Locate and identify every blood parasite.
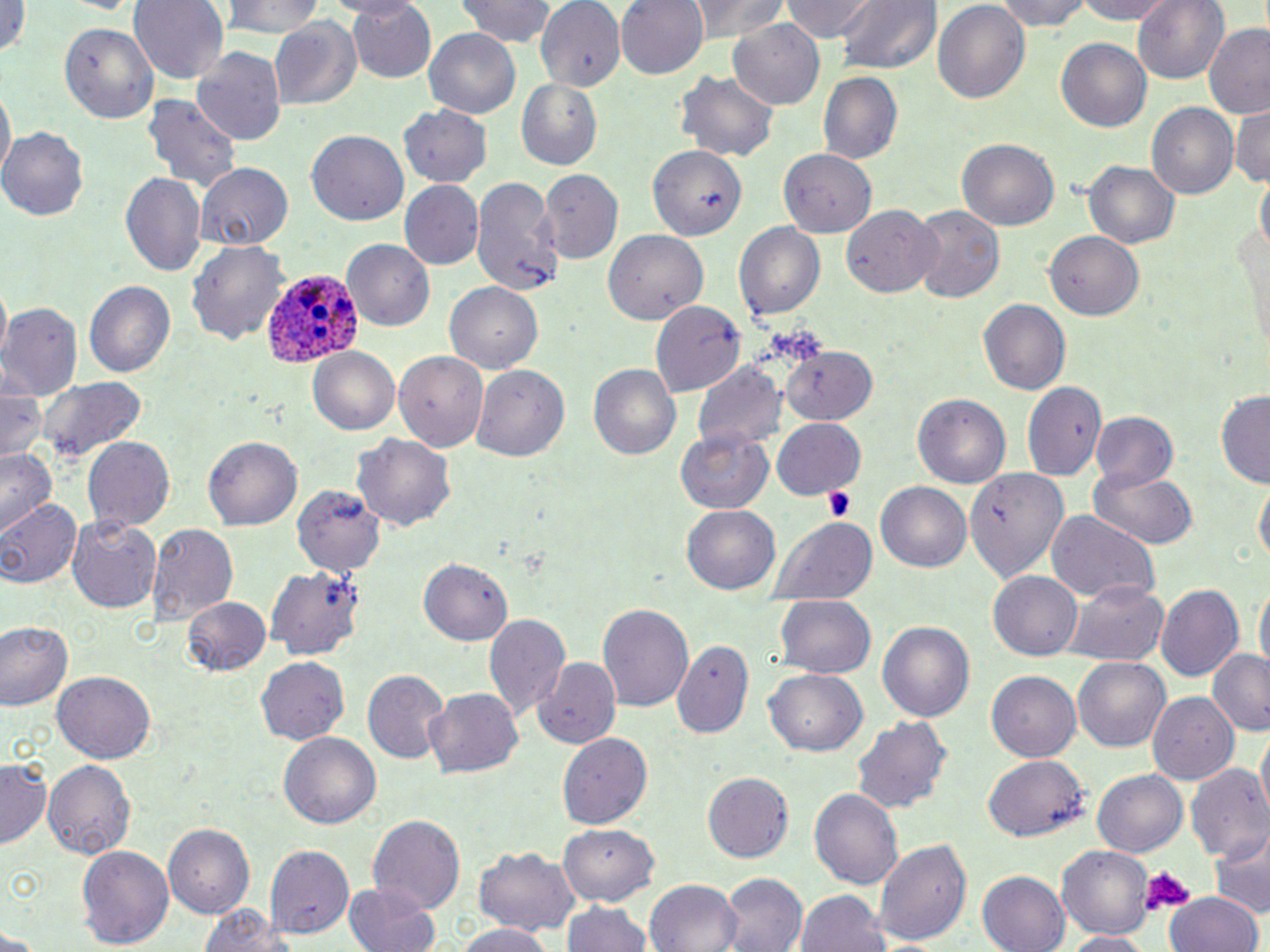
Approximate bounding boxes as (x1, y1, x2, y2) in pixels.
Plasmodium ovale-infected red blood cells: (258, 269, 367, 371).
No Plasmodium falciparum, Plasmodium malariae, Plasmodium vivax, Babesia divergens, or Trypanosoma brucei observed.

Platelet locations: (824, 488, 855, 523), (1140, 865, 1194, 913). Uninfected red blood cell locations: (129, 0, 228, 84), (221, 0, 329, 38), (343, 0, 436, 84), (454, 0, 558, 47), (614, 0, 709, 80), (686, 0, 789, 44), (778, 0, 875, 42), (830, 0, 940, 75), (932, 0, 1032, 105), (992, 0, 1097, 31), (1068, 0, 1179, 23), (1133, 0, 1230, 87), (534, 2, 626, 85), (0, 3, 25, 63), (269, 19, 364, 110), (727, 19, 825, 108), (58, 20, 159, 126), (1203, 24, 1270, 120), (423, 29, 523, 118), (1056, 38, 1151, 133), (194, 45, 286, 145), (674, 70, 782, 162), (818, 73, 905, 163), (517, 81, 603, 170), (1, 91, 13, 181), (141, 93, 245, 197), (1147, 104, 1236, 200), (1232, 104, 1270, 190), (1180, 105, 1270, 194), (399, 106, 492, 188), (2, 129, 88, 219), (306, 129, 408, 225), (957, 137, 1059, 231), (648, 143, 747, 241), (779, 148, 876, 238), (1084, 158, 1181, 249), (196, 163, 293, 249), (542, 170, 622, 262), (121, 172, 206, 278), (470, 176, 558, 293), (399, 180, 484, 267), (841, 204, 943, 298), (910, 204, 1004, 305), (1235, 212, 1270, 359), (734, 221, 827, 321), (1044, 230, 1144, 320), (606, 231, 709, 323), (341, 240, 435, 332), (189, 241, 289, 346), (85, 281, 177, 379), (446, 281, 545, 371), (649, 299, 745, 396), (978, 299, 1070, 396), (2, 304, 83, 397), (782, 346, 880, 425), (307, 348, 402, 436), (394, 352, 488, 452), (587, 361, 681, 461), (693, 362, 786, 455), (473, 365, 570, 461), (34, 374, 147, 463), (1027, 383, 1106, 481), (2, 385, 48, 462), (1215, 392, 1270, 490), (913, 394, 1009, 489), (1089, 413, 1181, 496), (772, 416, 865, 500), (675, 428, 774, 514), (354, 432, 457, 534), (205, 436, 304, 531), (83, 437, 175, 533), (0, 446, 58, 532), (963, 466, 1070, 583), (1088, 469, 1201, 549), (1254, 477, 1269, 566), (294, 483, 385, 576), (875, 483, 972, 574), (0, 496, 84, 587), (682, 503, 783, 595), (1046, 512, 1159, 605), (66, 514, 159, 612), (771, 515, 880, 606), (145, 522, 237, 623), (420, 559, 512, 644), (266, 564, 364, 662), (989, 571, 1083, 662), (1254, 580, 1269, 676), (1064, 582, 1170, 664), (1155, 583, 1244, 685), (183, 596, 271, 676), (774, 596, 876, 680), (596, 603, 693, 716), (485, 611, 570, 721), (877, 619, 976, 725), (2, 621, 73, 711), (673, 639, 755, 741), (1208, 648, 1270, 737), (257, 658, 349, 744), (533, 658, 620, 747), (1073, 659, 1171, 752), (765, 668, 866, 757), (362, 669, 450, 764), (53, 671, 156, 761), (987, 673, 1080, 761), (425, 686, 524, 778), (1150, 695, 1239, 782), (853, 716, 952, 817), (279, 732, 380, 829), (557, 733, 652, 831), (1256, 733, 1269, 819), (985, 757, 1089, 842), (0, 758, 51, 846), (43, 759, 136, 860), (1185, 761, 1270, 864), (1090, 771, 1189, 858), (705, 772, 794, 864), (810, 786, 904, 891), (368, 813, 466, 918), (164, 824, 255, 918), (559, 824, 659, 903), (1212, 828, 1270, 917), (874, 836, 975, 947), (265, 842, 354, 940), (77, 843, 175, 949), (1058, 845, 1152, 939), (473, 848, 583, 937), (978, 871, 1069, 952), (721, 872, 808, 952), (646, 877, 743, 952), (344, 880, 442, 952), (794, 890, 892, 952), (1166, 892, 1264, 952), (560, 900, 656, 952), (196, 902, 297, 952), (452, 922, 555, 952), (1061, 931, 1155, 952). Slide-level diagnosis: Plasmodium ovale. Light microscopy. 1000x magnification. Thin blood smear. Single field of view. Image is 1270×952 pixels. May-Grünwald-Giemsa stain.